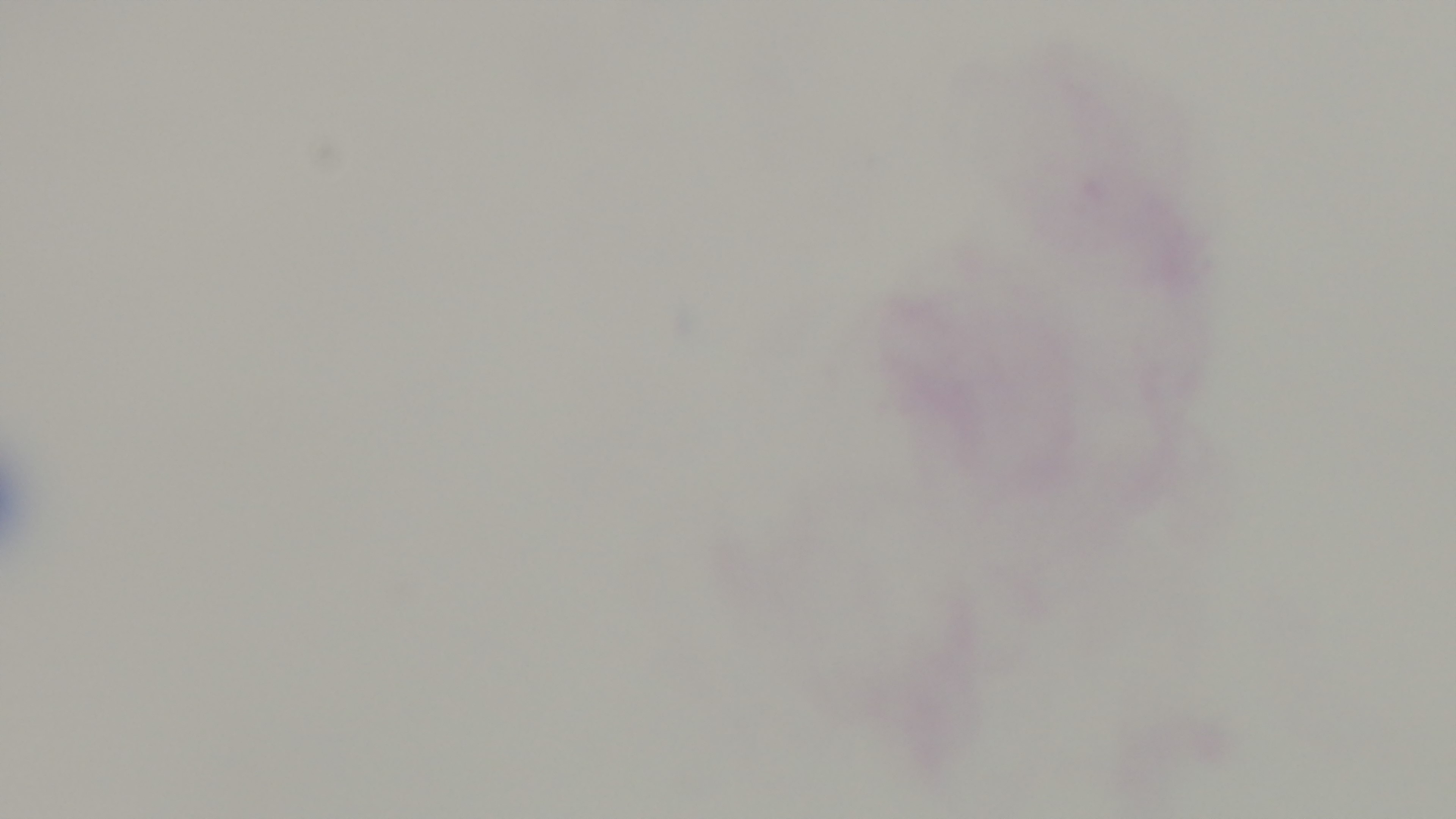
{
  "objective": "100x oil immersion",
  "stain": "Giemsa",
  "capture": "mounted 4K digital camera",
  "preparation": "thick blood film",
  "malaria_status": "negative",
  "modality": "light microscopy",
  "field_of_view": "single"
}